Assess this cell for malaria.
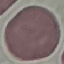
Uninfected.

Summary:
  - Capture: smartphone camera at the microscope eyepiece
  - Preparation: thin blood smear
  - Image type: automatically extracted cell patch, resized to 64 × 64 pixels
  - Stain: Giemsa